Identify the parasite.
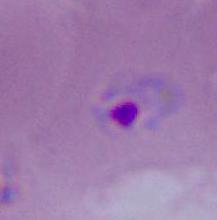
This is Plasmodium.

Summary:
  - Modality: micrograph
  - Magnification: 400x or 1000x